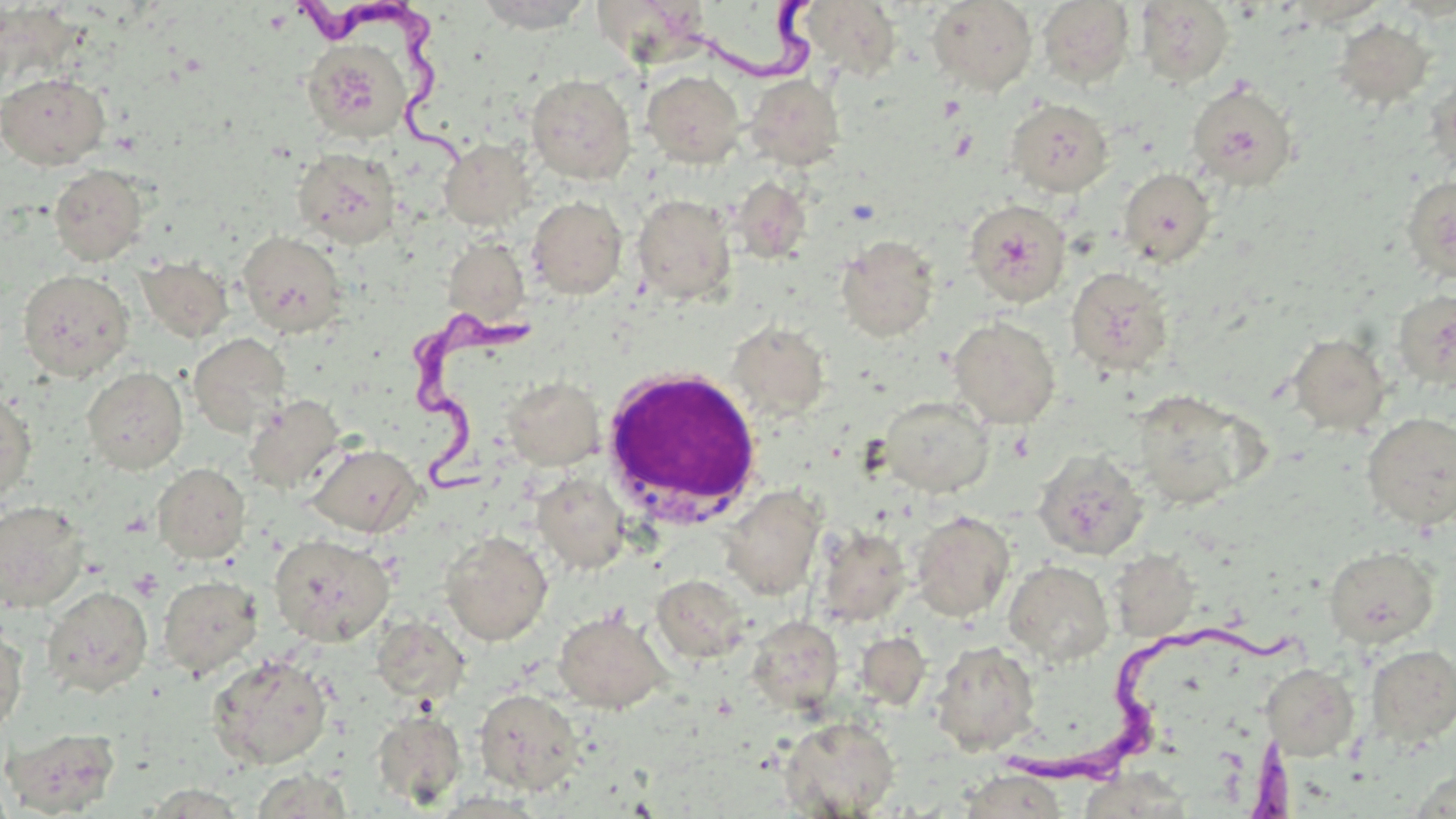
Approximate bounding boxes as named x1/y1/x2/y2 corners in pixels. Uninfected red blood cell locations: (x1=476, y1=0, x2=594, y2=33), (x1=591, y1=0, x2=708, y2=66), (x1=799, y1=0, x2=902, y2=82), (x1=927, y1=1, x2=1037, y2=95), (x1=1037, y1=1, x2=1135, y2=88), (x1=1135, y1=1, x2=1235, y2=87), (x1=1333, y1=19, x2=1434, y2=109), (x1=302, y1=39, x2=412, y2=143), (x1=641, y1=70, x2=745, y2=167), (x1=0, y1=72, x2=110, y2=169), (x1=525, y1=73, x2=636, y2=183), (x1=745, y1=73, x2=845, y2=171), (x1=1186, y1=80, x2=1300, y2=191), (x1=1005, y1=98, x2=1114, y2=197), (x1=440, y1=138, x2=535, y2=230), (x1=292, y1=146, x2=402, y2=248), (x1=49, y1=165, x2=148, y2=266), (x1=1118, y1=168, x2=1216, y2=267), (x1=1401, y1=175, x2=1456, y2=282), (x1=729, y1=176, x2=812, y2=264), (x1=632, y1=194, x2=737, y2=304), (x1=527, y1=196, x2=627, y2=299), (x1=964, y1=200, x2=1073, y2=306), (x1=238, y1=231, x2=347, y2=338), (x1=442, y1=235, x2=530, y2=329), (x1=836, y1=235, x2=939, y2=342), (x1=137, y1=257, x2=234, y2=342), (x1=1066, y1=267, x2=1174, y2=375), (x1=17, y1=269, x2=135, y2=381), (x1=1392, y1=289, x2=1456, y2=391), (x1=948, y1=316, x2=1060, y2=428), (x1=727, y1=321, x2=830, y2=422), (x1=187, y1=333, x2=290, y2=437), (x1=1288, y1=333, x2=1391, y2=435), (x1=82, y1=366, x2=188, y2=474), (x1=503, y1=376, x2=604, y2=469), (x1=0, y1=388, x2=37, y2=504), (x1=1131, y1=389, x2=1256, y2=508), (x1=244, y1=393, x2=346, y2=494), (x1=878, y1=396, x2=993, y2=497), (x1=1362, y1=412, x2=1456, y2=529), (x1=307, y1=443, x2=423, y2=537), (x1=1033, y1=448, x2=1149, y2=560), (x1=153, y1=463, x2=250, y2=563), (x1=532, y1=472, x2=630, y2=574), (x1=720, y1=485, x2=826, y2=600), (x1=0, y1=499, x2=90, y2=613), (x1=910, y1=510, x2=1015, y2=622), (x1=813, y1=524, x2=912, y2=627), (x1=440, y1=531, x2=553, y2=646), (x1=269, y1=534, x2=394, y2=646), (x1=1323, y1=545, x2=1439, y2=649), (x1=1109, y1=548, x2=1200, y2=642), (x1=1004, y1=560, x2=1114, y2=666), (x1=652, y1=574, x2=750, y2=663), (x1=158, y1=575, x2=263, y2=679), (x1=42, y1=585, x2=152, y2=697), (x1=553, y1=610, x2=670, y2=713), (x1=746, y1=616, x2=844, y2=714), (x1=371, y1=617, x2=471, y2=705), (x1=0, y1=621, x2=28, y2=737), (x1=856, y1=632, x2=931, y2=709), (x1=930, y1=640, x2=1041, y2=754), (x1=1366, y1=644, x2=1456, y2=746), (x1=208, y1=653, x2=333, y2=769), (x1=1260, y1=663, x2=1359, y2=760), (x1=474, y1=688, x2=583, y2=796), (x1=371, y1=702, x2=584, y2=805), (x1=371, y1=708, x2=468, y2=810), (x1=779, y1=716, x2=900, y2=817), (x1=2, y1=726, x2=122, y2=816), (x1=249, y1=769, x2=357, y2=818), (x1=958, y1=771, x2=1070, y2=818), (x1=135, y1=784, x2=253, y2=817). Platelet locations: (x1=128, y1=569, x2=163, y2=600). White blood cell locations: (x1=599, y1=367, x2=763, y2=525). Trypanosoma brucei locations: (x1=686, y1=0, x2=834, y2=96), (x1=294, y1=3, x2=469, y2=174), (x1=409, y1=304, x2=547, y2=517), (x1=1008, y1=612, x2=1300, y2=786), (x1=1243, y1=734, x2=1299, y2=819). Slide-level diagnosis: Trypanosoma brucei. One field of a larger specimen. Thin blood smear. Image is 1456×819 pixels. Light microscopy. Captured at 1000x magnification. May-Grünwald-Giemsa-stained preparation.